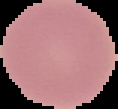

From a thin blood smear. Malaria status: uninfected. Image is 118×109 pixels. The area outside the segmented cell region is set to black.